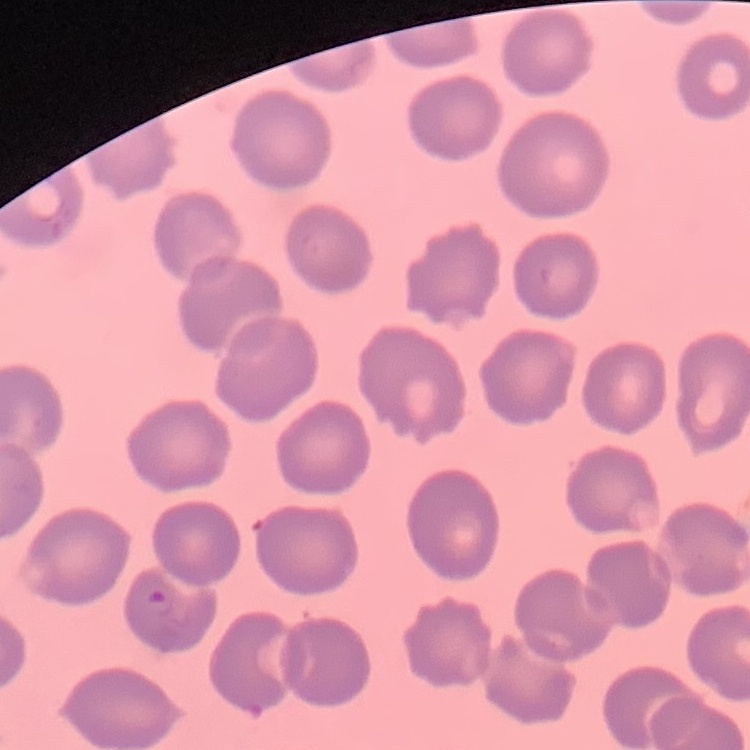

Summary:
  - Red blood cell morphology: no rouleaux formation
  - Preparation: thin peripheral smear
  - Stain: Field's or Giemsa
  - Image type: one tile cut from a larger photomicrograph